Name the parasite shown.
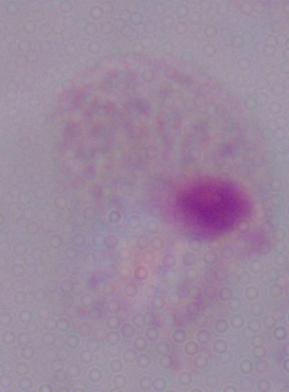
This is a trichomonad.

Captured at 1000x magnification. Photomicrograph.